Classify this cell by malaria status.
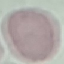
It is uninfected.

Summary:
  - Preparation: thin blood smear
  - Stain: Giemsa
  - Image type: automatically extracted cell patch, resized to 64 × 64 pixels
  - Capture: smartphone camera at the microscope eyepiece